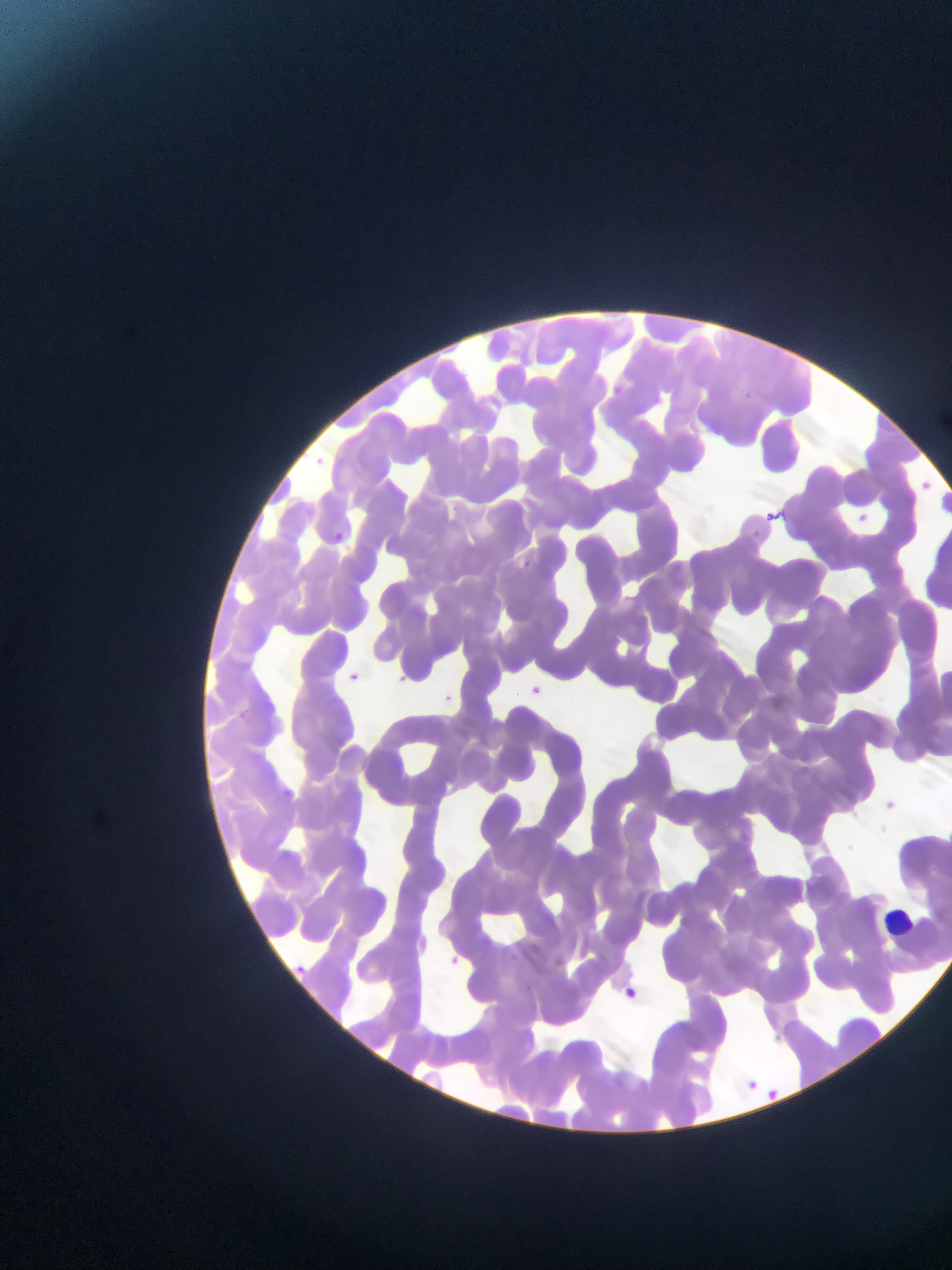
capture: mobile-phone photograph through a microscope
leukocyte_locations: 'approximate bounding boxes as left top right bottom in pixels: 879 902 914 941'
image_size: 952×1270 pixels
field_of_view: single
country: Ghana
malaria_parasite_locations: 'approximate bounding boxes as left top right bottom in pixels: 608 383 626 400; 306 454 328 473; 915 476 935 496; 853 508 872 525; 763 509 779 523; 328 529 348 547; 467 532 481 545; 519 558 532 570; 343 671 361 687; 393 673 408 686; 527 683 544 698; 441 690 457 705; 235 708 251 722; 280 787 295 801; 878 797 901 817; 445 953 462 969; 287 961 312 983; 616 984 644 1006; 737 1074 763 1098; 760 1084 785 1106'
preparation: thin blood film